Locate every uninfected red blood cell.
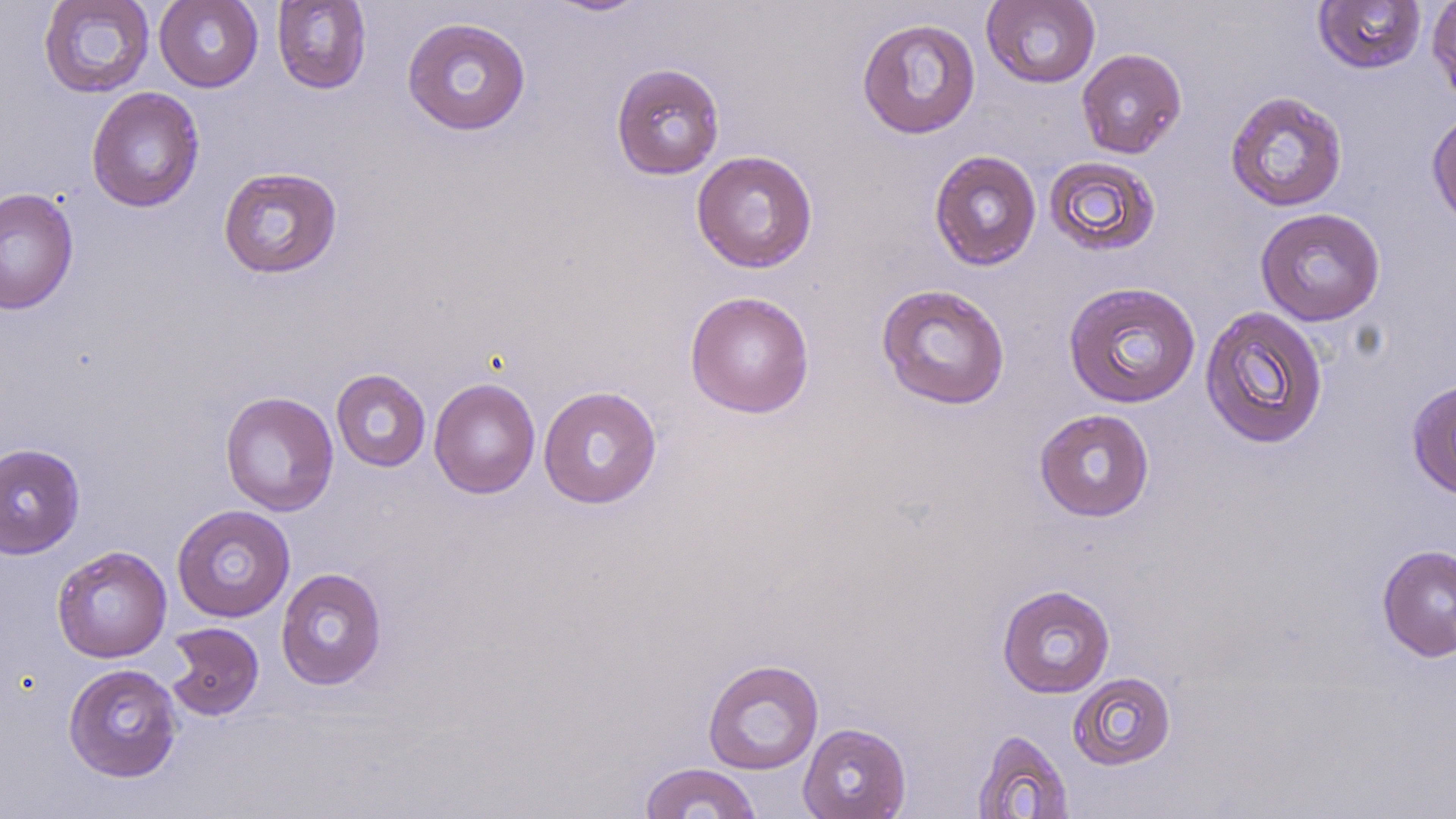
Approximate bounding boxes as (x1,y1)-(x2,y2) corner pairs in pixels.
Uninfected red blood cells: (38,0)-(155,99), (154,0)-(263,92), (540,0)-(653,18), (981,0)-(1101,89), (1427,0)-(1456,105), (272,1)-(372,94), (1312,1)-(1428,75), (402,17)-(531,136), (857,17)-(981,139), (1076,48)-(1187,159), (610,63)-(725,180), (86,86)-(205,212), (1225,90)-(1348,212), (1426,107)-(1456,232), (691,150)-(818,273), (928,150)-(1042,271), (1043,155)-(1161,257), (217,166)-(343,280), (0,186)-(79,315), (1255,207)-(1386,326), (1063,280)-(1201,409), (875,283)-(1011,410), (684,291)-(815,419), (1199,304)-(1329,450), (331,369)-(431,472), (429,377)-(541,499), (1406,378)-(1456,500), (538,386)-(663,509), (219,390)-(339,517), (1033,408)-(1155,522), (0,443)-(86,559), (171,504)-(295,623), (1376,544)-(1456,662), (51,545)-(172,663), (275,567)-(388,691), (996,584)-(1115,698), (164,621)-(265,721), (701,659)-(824,775), (62,663)-(183,783), (1068,671)-(1177,771), (797,722)-(911,819), (970,729)-(1074,817), (638,762)-(763,818).

Summary:
  - Slide-level diagnosis: no evidence of blood parasites
  - Field of view: single
  - Image size: 1456×819 pixels
  - Modality: optical microscopy
  - Magnification: 1000x
  - Preparation: thin blood smear
  - Stain: May-Grünwald-Giemsa